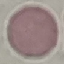
{
  "result": "no malaria parasites seen",
  "capture": "smartphone camera at the microscope eyepiece",
  "image_type": "automatically extracted cell patch, resized to 64 × 64 pixels",
  "stain": "Giemsa",
  "preparation": "thin blood smear"
}